Locate every leukocyte (white blood cell).
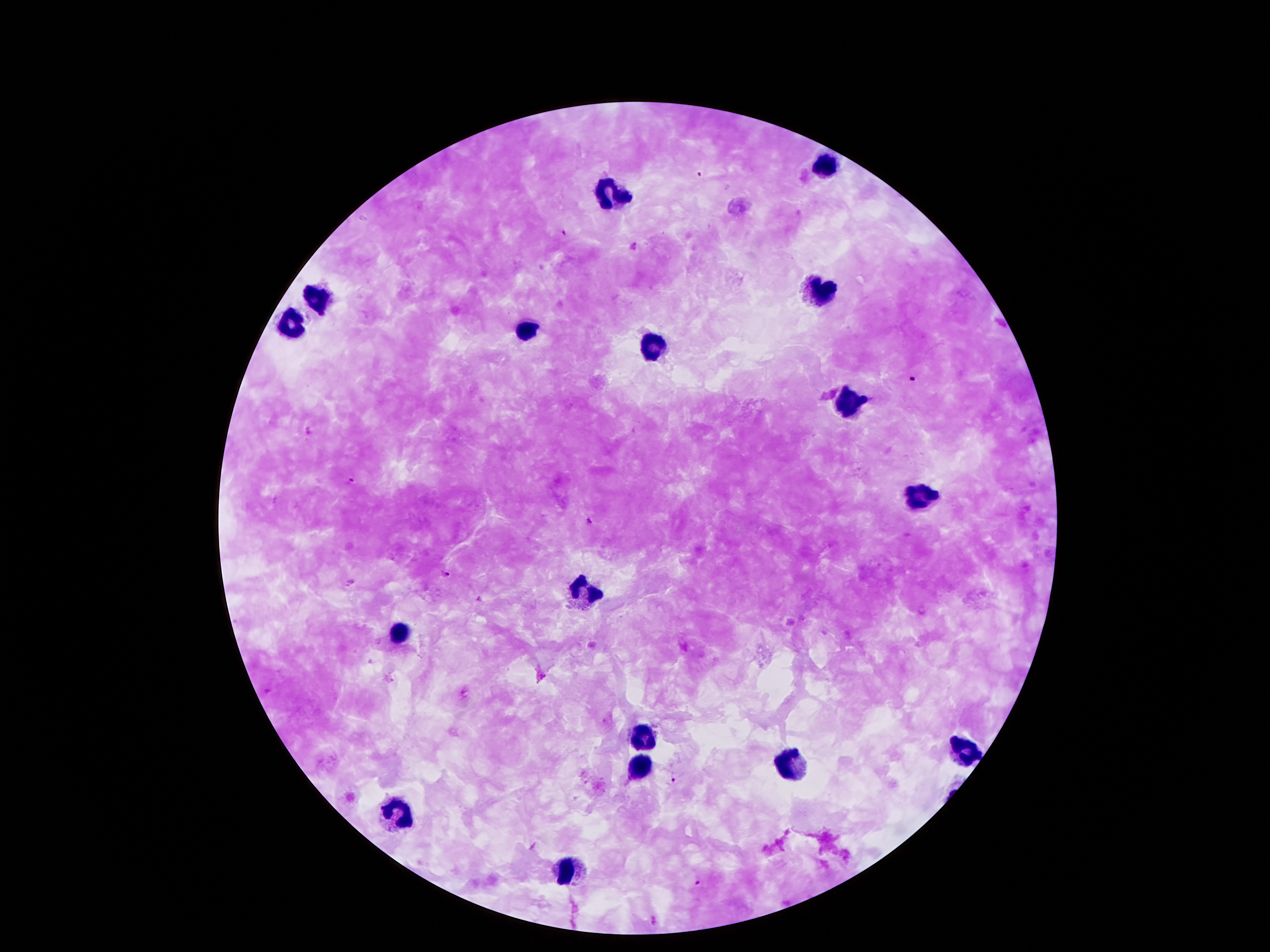
Approximate centers as [x, y] in pixels.
Leukocytes: [825, 164], [613, 191], [821, 292], [316, 299], [294, 324], [526, 331], [652, 349], [850, 399], [917, 497], [578, 594], [398, 632], [645, 734], [964, 749], [640, 766], [791, 767], [400, 809], [568, 872].

Plasmodium parasite locations: [563, 232], [911, 378], [308, 431], [350, 480], [589, 521], [446, 574], [268, 691], [672, 781], [698, 881]. Single field of view. Image is 1270×952 pixels. Giemsa-stained preparation. Smartphone photograph taken through the microscope eyepiece. Thick blood film. Patient malaria status: positive for Plasmodium falciparum. 100x magnification.